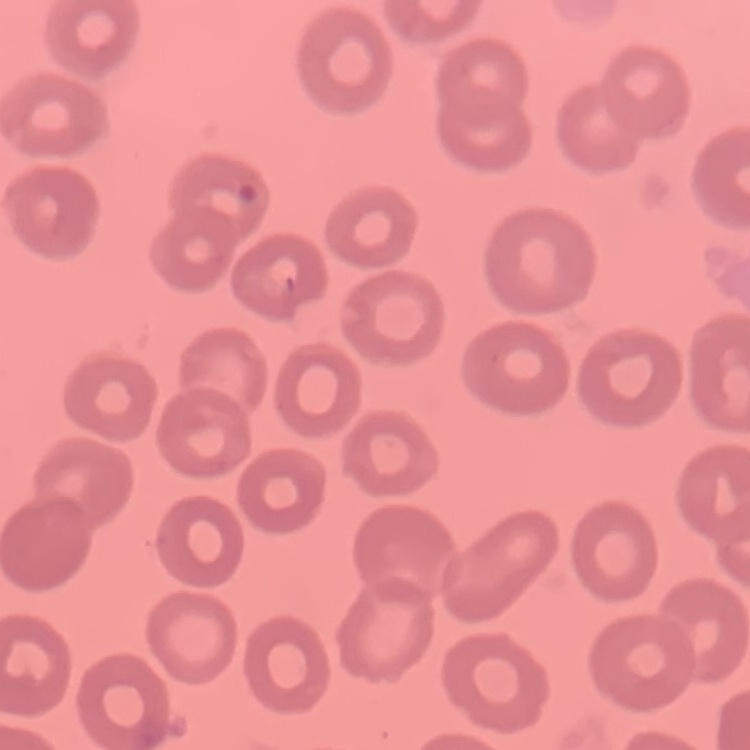

red blood cell morphology = no rouleaux formation
stain = Field's or Giemsa
image type = one tile cut from a larger photomicrograph
preparation = thin peripheral smear